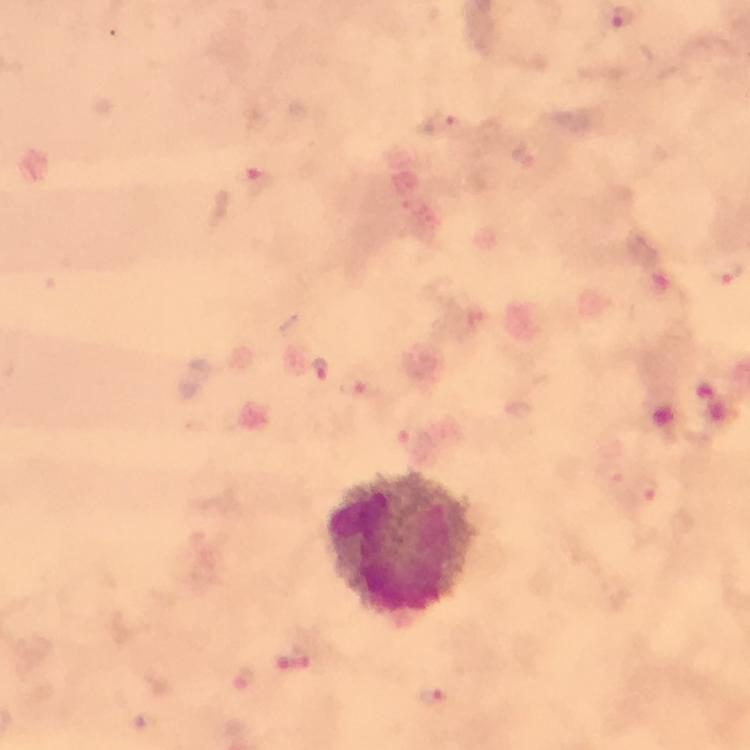

Approximate object centers, in pixels from the top-left corner. Leukocyte locations: (x=399, y=545). Plasmodium parasite locations: (x=624, y=20), (x=443, y=122), (x=260, y=182), (x=320, y=369), (x=360, y=384), (x=409, y=434), (x=616, y=472), (x=648, y=490), (x=244, y=678), (x=434, y=701). Immersion oil was used. Thick smear. Smartphone photograph taken through a microscope. From a diagnostic examination for malaria. Image is 750×750 pixels. 100x magnification. A crop from one field of view. Giemsa-stained preparation.